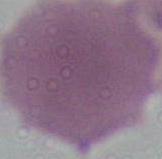

An erythrocyte is shown. 1000x magnification. Photomicrograph.